Comment on the morphology of the erythrocytes.
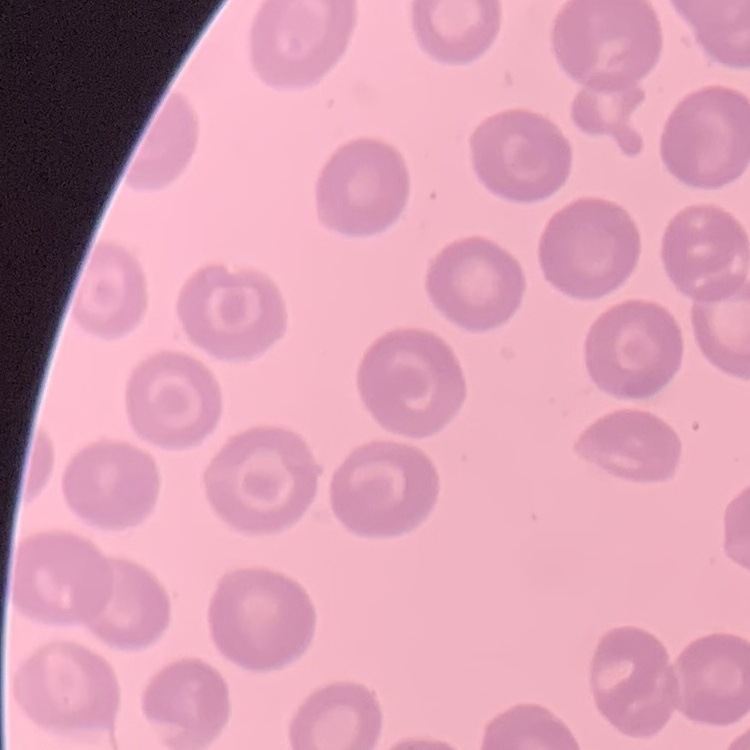
They show no rouleaux formation.

stain = Field's or Giemsa
image type = square crop of a larger photomicrograph
preparation = thin blood smear